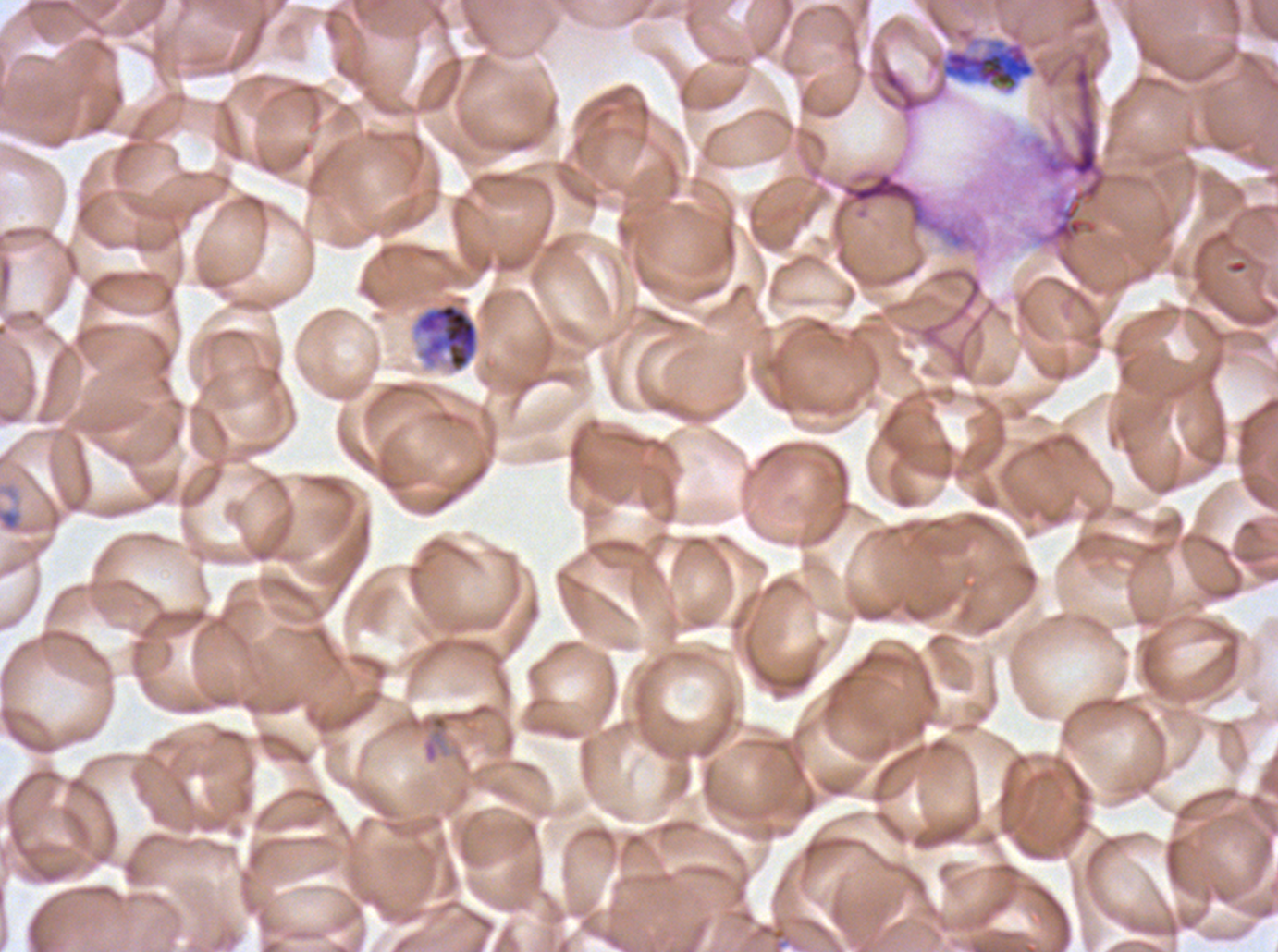

Approximate bounding boxes as {x1, y1, x2, y2} in pixels. Ring locations: {0, 507, 22, 532}. Debris locations: {831, 169, 977, 249}. Early schizont locations: {412, 301, 480, 373}. Segmenter locations: {874, 36, 1042, 108}. Life-cycle stages observed: ring, early schizont, segmenter. Image is 1278×952 pixels. Plasmodium falciparum cultured ex vivo for 24 to 48 hours, from a patient in The Gambia. One sub-image of a larger composite. Thin blood smear. Giemsa-stained preparation.